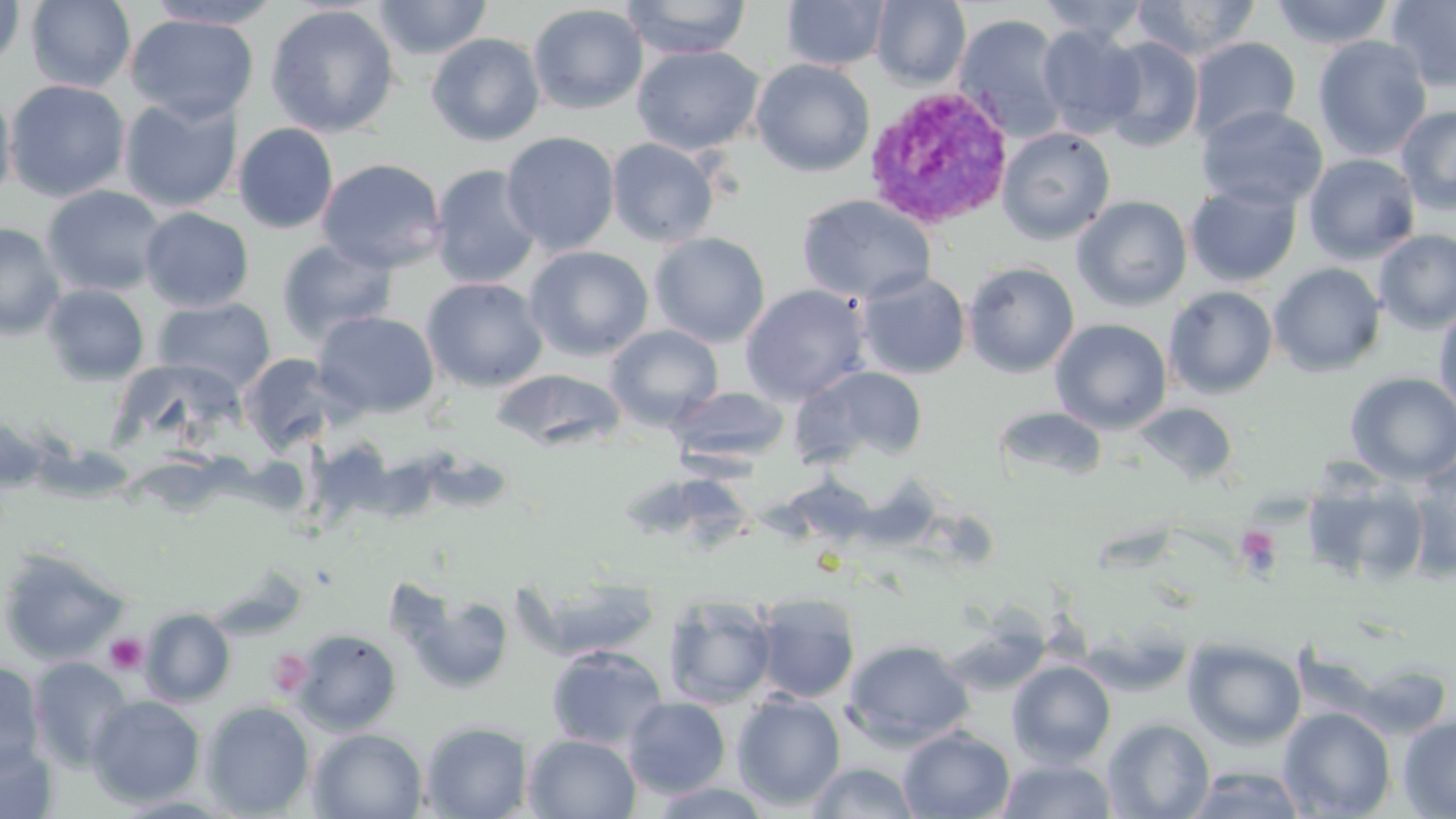
Approximate bounding boxes as [x1, y1, x2, y2] in pixels. Platelet locations: [1237, 526, 1280, 572], [104, 634, 148, 676]. Uninfected red blood cell locations: [0, 0, 25, 71], [25, 0, 136, 92], [144, 0, 284, 30], [373, 0, 492, 59], [620, 0, 752, 59], [871, 0, 971, 88], [1036, 0, 1151, 43], [1131, 0, 1263, 62], [1270, 0, 1395, 50], [1386, 0, 1456, 93], [782, 1, 891, 71], [528, 3, 648, 114], [265, 4, 400, 138], [1357, 8, 1452, 130], [125, 13, 259, 124], [954, 14, 1069, 141], [1037, 24, 1144, 137], [426, 33, 545, 146], [1312, 35, 1432, 161], [1188, 36, 1301, 143], [1099, 37, 1204, 152], [633, 45, 763, 155], [751, 59, 875, 177], [4, 79, 131, 202], [0, 86, 16, 205], [119, 97, 243, 213], [1197, 104, 1328, 210], [1395, 105, 1456, 215], [233, 123, 339, 234], [997, 127, 1115, 244], [501, 131, 620, 256], [606, 138, 719, 247], [1303, 153, 1421, 264], [316, 158, 446, 273], [429, 165, 542, 289], [1184, 182, 1302, 288], [42, 185, 167, 297], [796, 194, 936, 305], [1072, 196, 1193, 312], [140, 207, 254, 312], [0, 222, 65, 338], [1374, 229, 1456, 335], [649, 232, 770, 347], [276, 238, 397, 344], [524, 246, 654, 361], [963, 261, 1080, 377], [1268, 263, 1386, 377], [856, 271, 971, 380], [421, 277, 549, 392], [42, 283, 150, 385], [740, 284, 869, 406], [1164, 286, 1279, 399], [154, 297, 276, 393], [1434, 302, 1456, 421], [312, 310, 441, 419], [1050, 318, 1172, 434], [605, 324, 723, 428], [239, 353, 338, 454], [791, 364, 929, 467], [491, 368, 627, 452], [1345, 372, 1456, 485], [670, 386, 790, 466], [1134, 401, 1238, 485], [993, 406, 1108, 483], [0, 413, 49, 491], [1404, 460, 1456, 580], [1300, 470, 1431, 588], [0, 545, 129, 666], [519, 576, 663, 659], [390, 577, 516, 696], [753, 593, 861, 704], [663, 594, 778, 709], [141, 608, 235, 706], [942, 613, 1050, 696], [290, 629, 402, 735], [1183, 637, 1306, 750], [843, 638, 975, 750], [545, 644, 668, 751], [28, 657, 134, 772], [1007, 660, 1117, 767], [1351, 662, 1455, 738], [0, 663, 47, 777], [731, 693, 846, 810], [86, 695, 205, 806], [623, 696, 731, 798], [201, 700, 315, 817], [1278, 706, 1397, 818], [1398, 714, 1456, 817], [1102, 717, 1215, 818], [420, 720, 533, 818], [898, 726, 1015, 818], [309, 728, 427, 818], [523, 733, 641, 818], [0, 740, 58, 817], [996, 757, 1119, 818], [805, 761, 920, 818], [1184, 765, 1309, 818], [647, 782, 775, 818], [110, 793, 240, 818]. Plasmodium vivax-infected red blood cell locations: [863, 84, 1015, 230]. Slide-level diagnosis: Plasmodium vivax. Light microscopy. Thin blood smear. Image is 1456×819 pixels. One field of a larger specimen. Captured at 1000x magnification. May-Grünwald-Giemsa-stained preparation.